Classify this cell by malaria status.
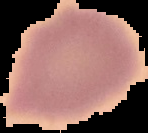
It is uninfected.

From a thin blood film. Image is 148×133 pixels. Segmented cell region on a black background.